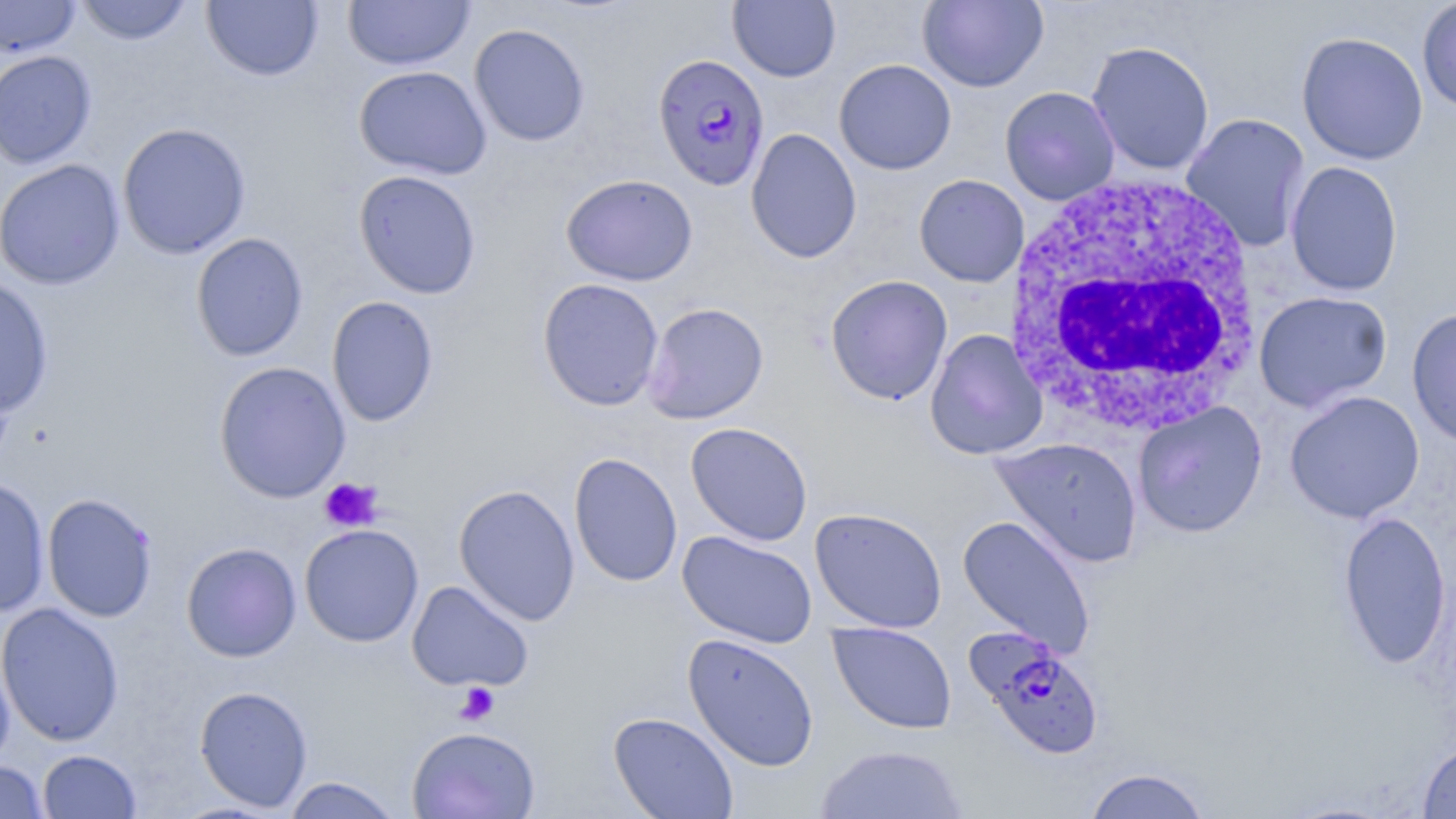
slide_level_diagnosis: Plasmodium falciparum
uninfected_red_blood_cell_locations: 'approximate bounding boxes as [x1, y1, x2, y2] in pixels: [0, 0, 81, 58], [74, 0, 194, 46], [201, 0, 323, 82], [918, 0, 1048, 92], [1416, 0, 1456, 113], [342, 1, 475, 71], [728, 1, 841, 82], [468, 23, 590, 147], [1295, 32, 1429, 165], [1086, 41, 1215, 176], [0, 49, 97, 170], [834, 59, 956, 175], [354, 65, 492, 180], [999, 86, 1120, 205], [1181, 113, 1311, 252], [117, 122, 252, 259], [745, 128, 862, 264], [0, 159, 126, 290], [1285, 161, 1403, 296], [354, 170, 482, 299], [561, 174, 698, 287], [914, 174, 1029, 287], [191, 232, 309, 362], [825, 274, 953, 405], [0, 275, 54, 417], [537, 278, 664, 411], [1254, 290, 1393, 412], [327, 296, 439, 427], [642, 302, 769, 424], [1406, 306, 1456, 446], [925, 328, 1048, 460], [213, 360, 351, 504], [1284, 390, 1424, 524], [1132, 401, 1268, 538], [685, 422, 813, 546], [990, 437, 1143, 569], [569, 452, 683, 588], [0, 477, 50, 618], [453, 484, 580, 626], [41, 493, 159, 622], [809, 507, 948, 633], [1337, 511, 1452, 668], [957, 515, 1097, 659], [300, 524, 424, 647], [677, 530, 817, 649], [181, 542, 302, 662], [406, 580, 534, 692], [0, 601, 125, 747], [828, 622, 957, 734], [682, 633, 820, 772], [0, 637, 15, 770], [194, 685, 313, 812], [608, 711, 739, 819], [406, 726, 540, 819], [1418, 742, 1456, 818], [815, 744, 970, 819], [37, 749, 142, 818], [0, 760, 49, 818], [1083, 768, 1213, 818], [280, 777, 403, 818]'
modality: optical microscopy
magnification: 1000x
field_of_view: one of a larger specimen
image_size: 1456×819 pixels
plasmodium_falciparum_infected_red_blood_cell_locations: 'approximate bounding boxes as [x1, y1, x2, y2] in pixels: [653, 52, 770, 192], [968, 630, 1105, 759]'
preparation: thin blood film
platelet_locations: 'approximate bounding boxes as [x1, y1, x2, y2] in pixels: [318, 477, 383, 532], [454, 682, 500, 725]'
stain: May-Grünwald-Giemsa
white_blood_cell_locations: 'approximate bounding boxes as [x1, y1, x2, y2] in pixels: [1004, 172, 1262, 435]'